Locate every malaria parasite and every leukocyte.
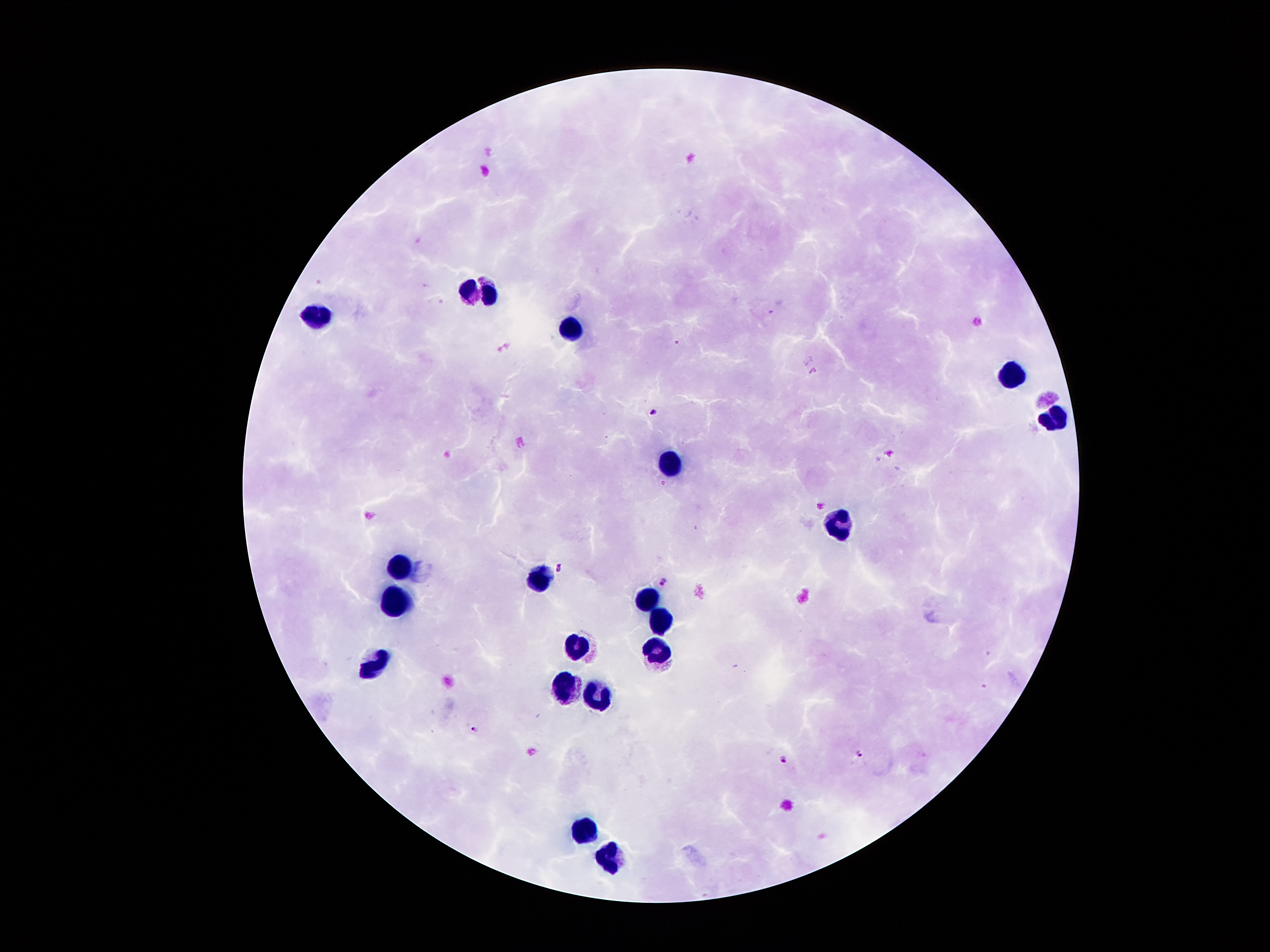

Approximate centers as [x, y] in pixels.
Malaria parasites: [424, 284], [770, 309], [676, 342], [814, 368], [652, 410], [663, 482], [556, 568], [663, 580], [476, 730], [858, 755], [781, 757].
Leukocytes: [480, 293], [315, 316], [567, 332], [1011, 375], [1055, 421], [668, 464], [839, 522], [403, 565], [539, 583], [644, 598], [394, 604], [660, 621], [575, 648], [657, 654], [376, 666], [565, 687], [601, 698], [583, 834], [610, 860].

{
  "image_size": "1270×952 pixels",
  "preparation": "thick blood film",
  "field_of_view": "one from this slide",
  "magnification": "100x",
  "patient_malaria_status": "infected with Plasmodium falciparum",
  "capture": "smartphone through the microscope eyepiece",
  "stain": "Giemsa"
}